Locate and identify every blood parasite.
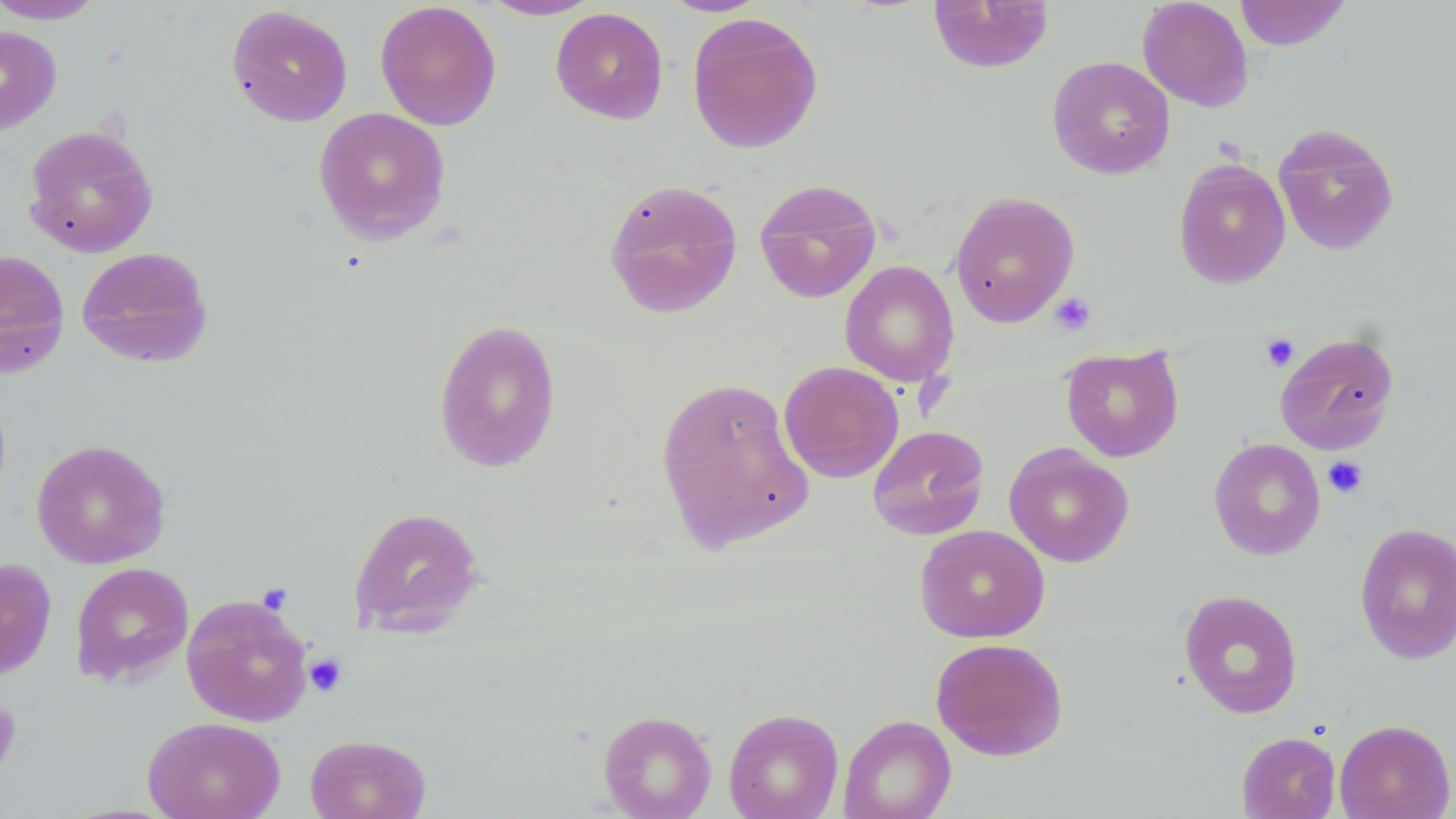
No blood parasites seen.

slide-level diagnosis = no evidence of blood parasites
field of view = one of a larger specimen
preparation = thin blood film
stain = May-Grünwald-Giemsa
image size = 1456×819 pixels
platelet locations = approximate bounding boxes as [x1, y1, x2, y2] in pixels: [1049, 292, 1096, 336], [1260, 333, 1299, 372], [1323, 456, 1368, 498], [305, 653, 347, 696], [0, 696, 23, 778]
magnification = 1000x
uninfected red blood cell locations = approximate bounding boxes as [x1, y1, x2, y2] in pixels: [659, 0, 769, 16], [928, 0, 1054, 74], [1137, 0, 1255, 112], [1234, 0, 1352, 51], [0, 1, 108, 24], [375, 1, 501, 131], [478, 1, 601, 21], [225, 5, 353, 127], [550, 7, 669, 124], [686, 12, 824, 154], [0, 25, 61, 135], [1047, 56, 1175, 180], [312, 107, 451, 245], [1273, 123, 1399, 256], [23, 124, 159, 258], [1173, 158, 1291, 289], [603, 178, 743, 319], [754, 178, 882, 303], [949, 191, 1080, 327], [75, 246, 214, 369], [0, 249, 70, 379], [840, 260, 959, 387], [433, 318, 562, 473], [1274, 331, 1399, 454], [1060, 345, 1184, 462], [779, 360, 904, 483], [654, 375, 814, 554], [867, 424, 990, 540], [31, 438, 170, 569], [1208, 438, 1325, 560], [1004, 443, 1135, 567], [348, 505, 486, 637], [1354, 522, 1456, 665], [914, 525, 1050, 643], [0, 558, 57, 680], [70, 562, 193, 687], [1178, 589, 1304, 719], [181, 592, 314, 727], [930, 637, 1068, 761], [723, 708, 844, 819], [598, 709, 717, 819], [838, 714, 957, 819], [142, 715, 286, 819], [1334, 718, 1455, 819], [1236, 731, 1341, 819], [305, 733, 432, 819]
modality = optical microscopy